Locate every Plasmodium parasite.
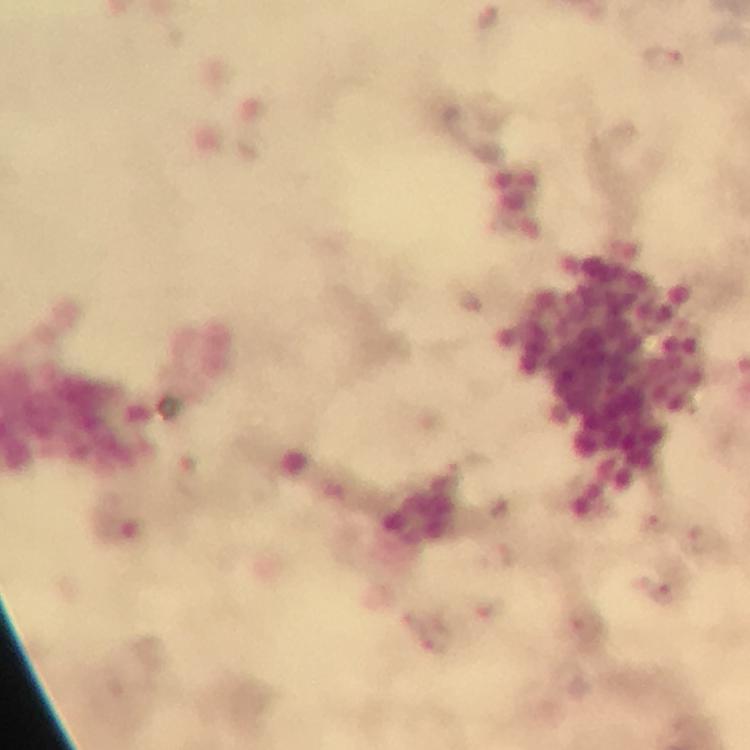
Approximate object centers, in pixels from the top-left corner.
Plasmodium parasites: (x=663, y=59).

image size = 750×750 pixels
immersion oil = used
capture = smartphone camera through the microscope
preparation = thick blood film
context = from a diagnostic examination for malaria
stain = Giemsa
magnification = 100x
cropped from = one field of view